Assess this cell for malaria.
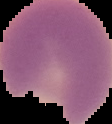

Parasitized.

Summary:
  - Image size: 112×124 pixels
  - Preparation: thin blood smear
  - Image type: segmented cell region on a black background